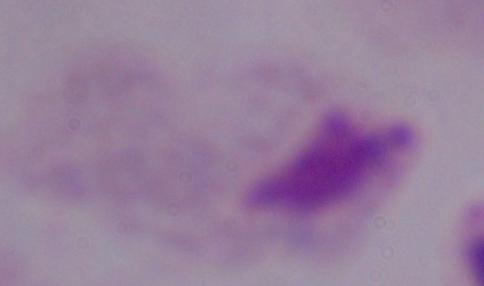 Captured at 1000x magnification. A trichomonad is shown. Micrograph.